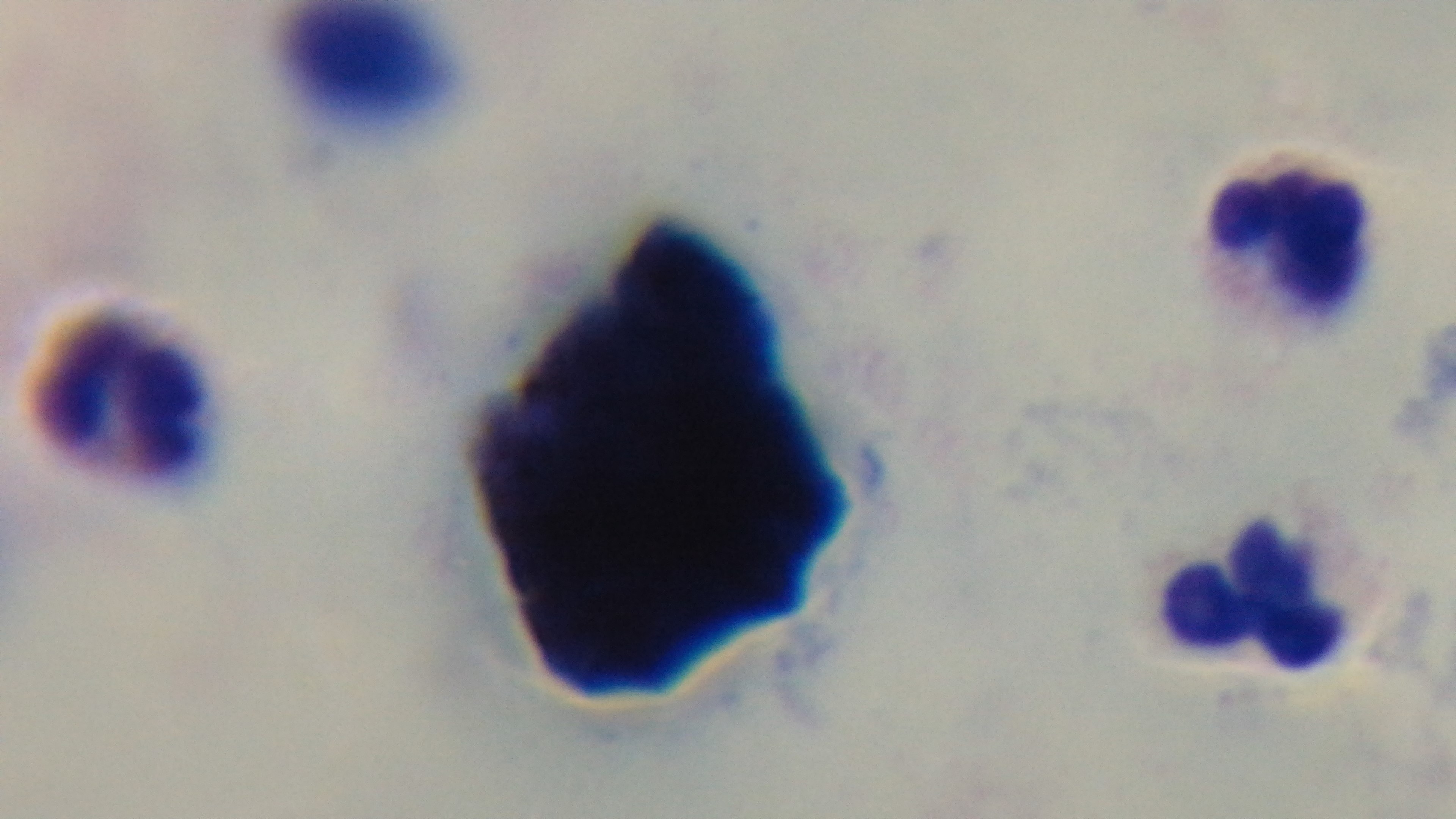

Photomicrograph. Giemsa stain. 100x oil-immersion objective. Captured with a mounted 4K digital camera. One field from the slide. Preparation: thick blood film. Malaria status: negative.